Give the extent of all Plasmodium vivax-infected red blood cells.
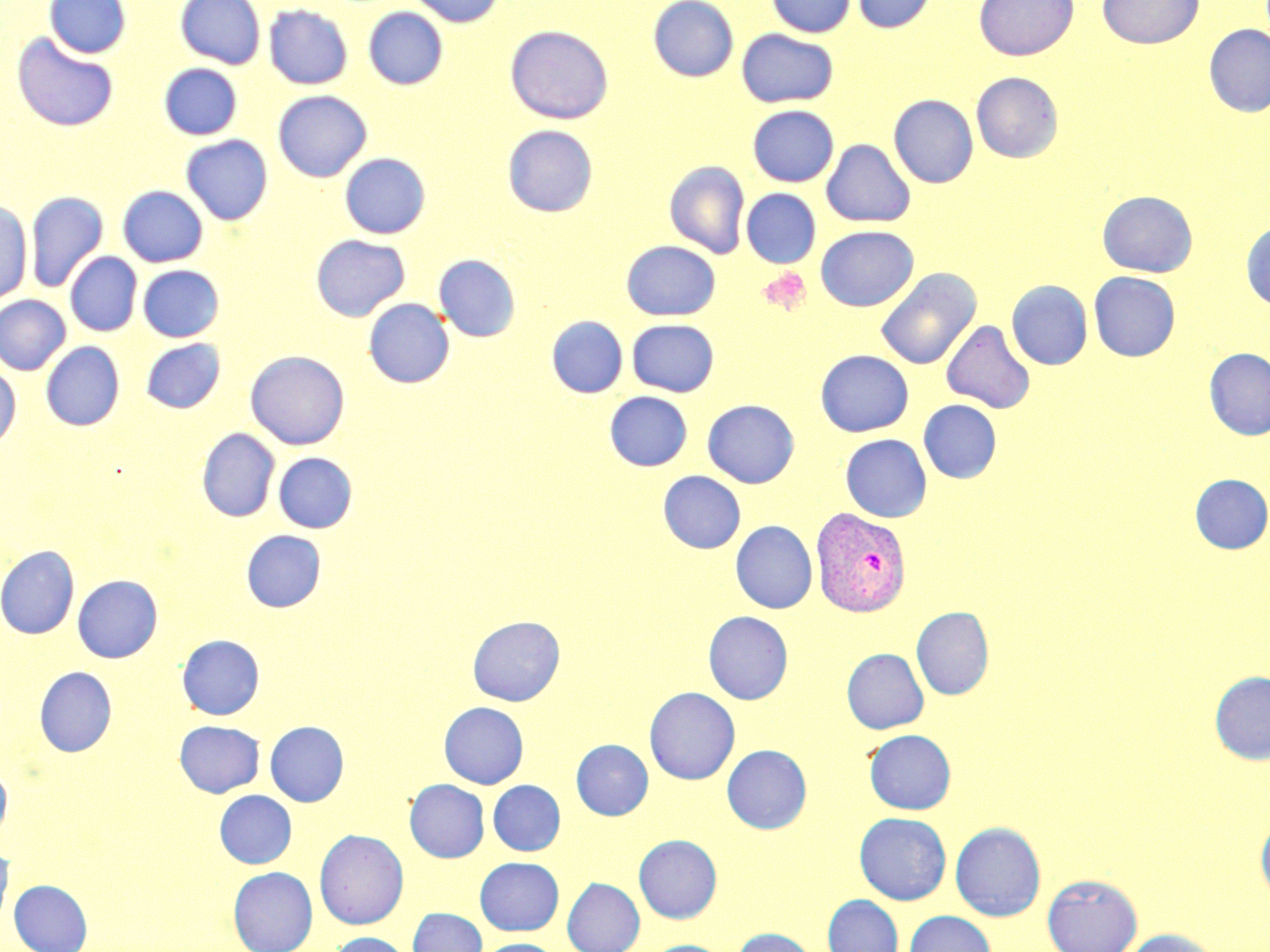

Approximate bounding boxes as (x1,y1)-(x2,y2) corner pairs in pixels.
Plasmodium vivax-infected red blood cells: (811,508)-(911,617).

Platelet locations: (759,267)-(812,316). Uninfected red blood cell locations: (44,0)-(131,58), (175,0)-(266,69), (409,0)-(504,27), (648,0)-(738,81), (766,0)-(856,38), (852,0)-(936,33), (973,0)-(1079,61), (1097,0)-(1203,49), (264,4)-(353,90), (363,7)-(448,90), (1203,24)-(1270,117), (505,25)-(614,124), (737,29)-(838,108), (12,31)-(119,132), (159,63)-(242,140), (971,72)-(1063,162), (272,90)-(372,182), (888,94)-(979,188), (747,105)-(838,187), (502,125)-(598,217), (180,135)-(273,225), (821,139)-(916,227), (340,153)-(430,239), (664,160)-(750,259), (118,185)-(208,267), (741,188)-(821,268), (1097,190)-(1197,278), (26,191)-(107,292), (0,202)-(31,305), (1241,221)-(1270,311), (816,225)-(918,311), (311,235)-(410,321), (622,240)-(721,320), (65,252)-(142,336), (434,254)-(521,342), (137,265)-(224,342), (876,267)-(981,371), (1089,271)-(1180,361), (1007,280)-(1092,370), (0,295)-(71,375), (364,298)-(454,388), (547,315)-(628,398), (627,319)-(719,397), (941,319)-(1035,414), (140,338)-(225,413), (41,341)-(124,431), (1203,348)-(1270,440), (815,349)-(914,437), (245,351)-(349,450), (0,363)-(21,448), (605,391)-(692,471), (702,399)-(799,488), (919,399)-(1002,483), (197,428)-(279,522), (840,434)-(932,522), (274,453)-(357,533), (658,471)-(745,553), (1190,474)-(1270,553), (730,521)-(817,613), (241,530)-(325,612), (0,545)-(79,639), (72,575)-(162,662), (911,607)-(994,700), (703,611)-(793,704), (468,615)-(565,706), (177,634)-(265,720), (842,648)-(929,733), (34,666)-(117,756), (1210,671)-(1270,764), (644,687)-(740,784), (439,702)-(528,788), (175,720)-(264,797), (265,721)-(349,806), (864,729)-(956,814), (571,739)-(653,820), (722,744)-(812,834), (0,763)-(12,845), (405,779)-(489,862), (488,780)-(565,856), (214,790)-(296,868), (854,812)-(951,905), (1256,815)-(1270,904), (950,822)-(1046,921), (314,828)-(409,929), (634,834)-(722,923), (0,843)-(14,926), (475,857)-(564,935), (228,867)-(318,952), (1042,874)-(1142,952), (562,878)-(644,952), (10,880)-(92,952), (822,895)-(903,952), (408,908)-(487,952), (904,911)-(996,952), (731,927)-(818,952), (1120,928)-(1222,952), (329,932)-(412,952), (476,938)-(562,952), (641,940)-(730,952). Slide-level diagnosis: Plasmodium vivax. Image is 1270×952 pixels. 1000x magnification. Light microscopy. Single field of view. Thin blood smear. May-Grünwald-Giemsa-stained preparation.